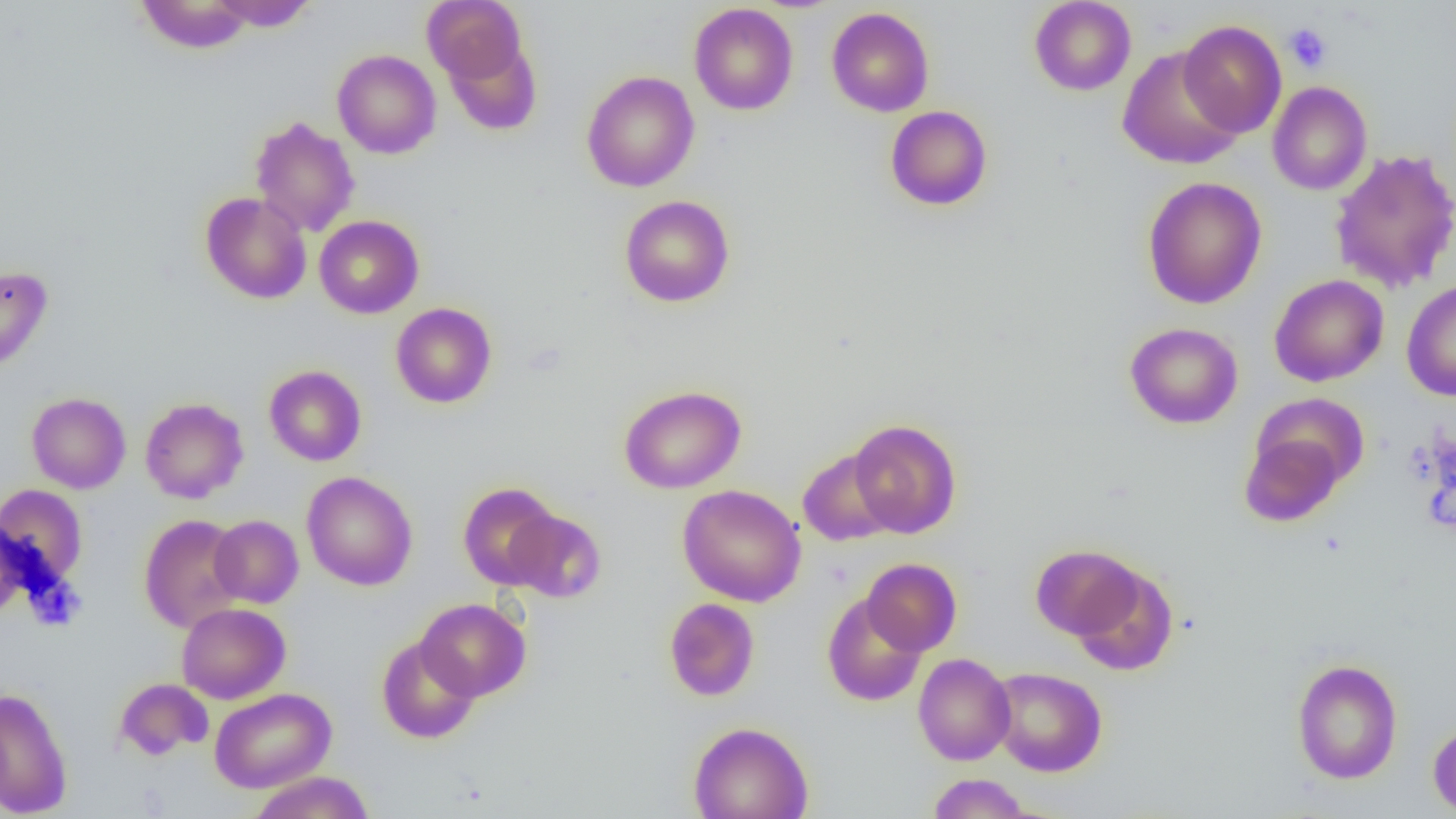
Summary:
  - Coordinate format: approximate bounding boxes as [x1, y1, x2, y2] in pixels
  - Platelet locations: [1283, 22, 1332, 73]
  - Uninfected red blood cell locations: [135, 0, 255, 54], [209, 0, 319, 32], [1029, 0, 1136, 96], [422, 1, 527, 86], [689, 3, 798, 116], [826, 7, 934, 117], [1178, 19, 1287, 137], [1117, 47, 1245, 170], [332, 49, 441, 159], [581, 70, 700, 192], [1267, 81, 1373, 196], [885, 105, 993, 211], [249, 116, 360, 238], [1329, 148, 1456, 294], [1141, 176, 1267, 309], [199, 191, 312, 304], [619, 195, 735, 308], [314, 215, 424, 319], [0, 265, 53, 372], [1269, 274, 1389, 387], [1401, 280, 1456, 401], [390, 302, 497, 409], [1124, 322, 1243, 429], [264, 365, 367, 466], [619, 385, 746, 493], [26, 392, 131, 494], [140, 397, 249, 503], [848, 419, 962, 538], [1239, 431, 1347, 527], [798, 448, 899, 546], [302, 471, 418, 590], [457, 482, 561, 590], [0, 484, 87, 586], [677, 485, 807, 607], [504, 508, 606, 603], [138, 513, 247, 632], [209, 515, 303, 608], [1030, 544, 1145, 641], [861, 558, 962, 656], [1068, 563, 1178, 676], [822, 593, 927, 707], [415, 598, 531, 701], [663, 598, 760, 701], [176, 602, 290, 703], [376, 635, 481, 744], [913, 653, 1016, 765], [1290, 658, 1403, 784], [988, 666, 1107, 776], [114, 678, 213, 761], [0, 686, 73, 818], [209, 688, 336, 793], [688, 721, 813, 819], [1427, 721, 1456, 816], [248, 771, 375, 819], [927, 774, 1032, 818]
  - Slide-level diagnosis: no evidence of blood parasites
  - Preparation: thin blood film
  - Modality: light microscopy
  - Field of view: one of a larger specimen
  - Magnification: 1000x
  - Image size: 1456×819 pixels